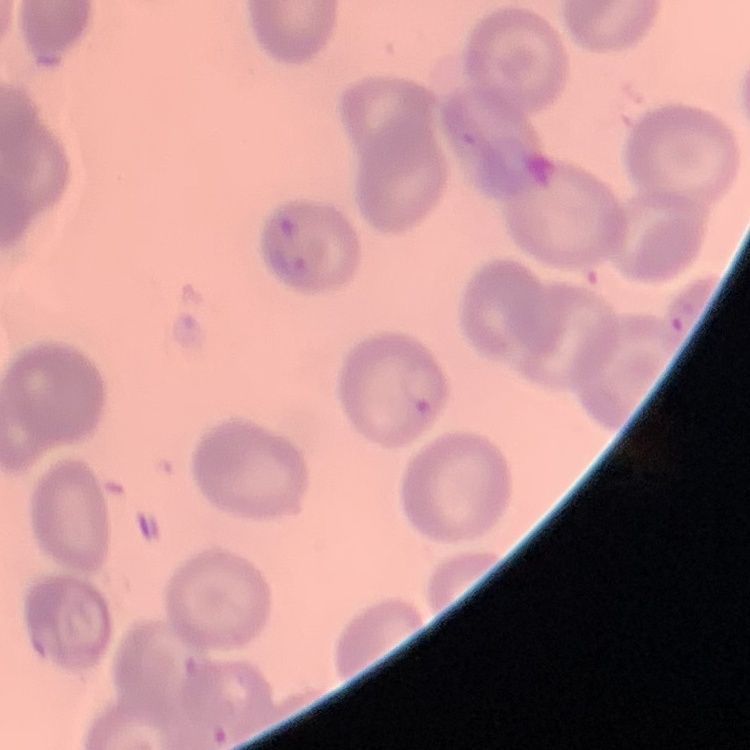

erythrocyte morphology = no rouleaux formation
image type = one tile cut from a larger photomicrograph
preparation = thin peripheral smear
stain = Field's or Giemsa